Comment on the morphology of the erythrocytes.
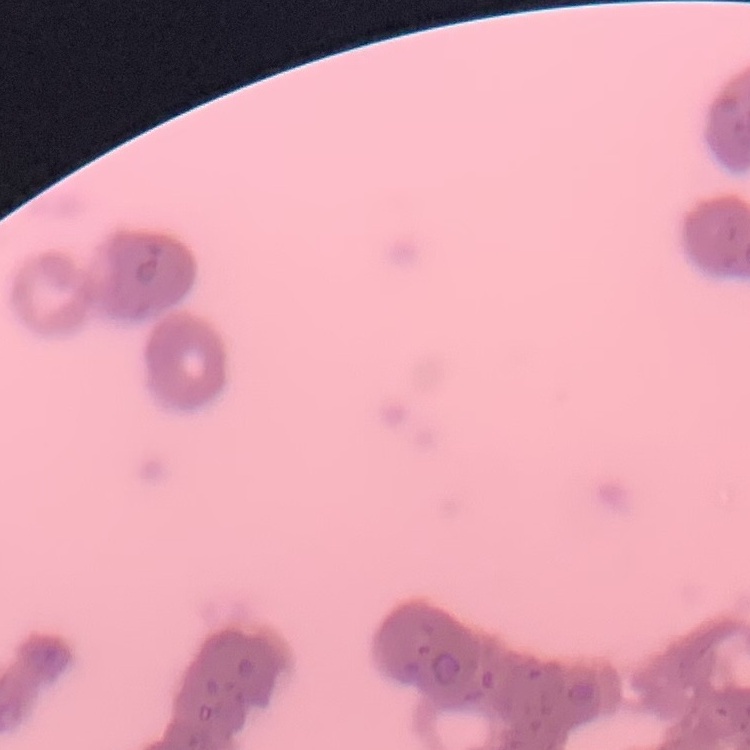
They show rouleaux formation.

Stained with either Field's or Giemsa. One tile cut from a larger photomicrograph. Thin blood film.